Classify this cell by malaria status.
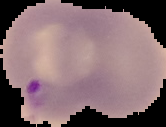

It is parasitized.

Summary:
  - Preparation: thin blood film
  - Image type: segmented cell region with the area outside set to black
  - Image size: 166×127 pixels